Classify this cell by malaria status.
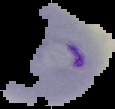
It is parasitized.

image_type: segmented cell region with the area outside set to black
preparation: thin blood smear
image_size: 115×109 pixels